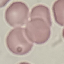

Result: negative for malaria parasites. Automatically extracted cell patch, resized to 64 × 64 pixels. Thin smear of blood. Photographed with a smartphone camera at the microscope eyepiece. Giemsa stain.